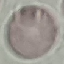
Result: no malaria parasites seen. Thin smear of blood. Giemsa-stained preparation. Automatically extracted cell patch, resized to 64 × 64 pixels. Acquired by smartphone through the microscope eyepiece.